Classify this cell by malaria status.
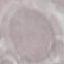

It is uninfected.

Giemsa-stained preparation. Automatically extracted cell patch, resized to 64 × 64 pixels. Acquired by smartphone through the microscope eyepiece. Thin blood film.